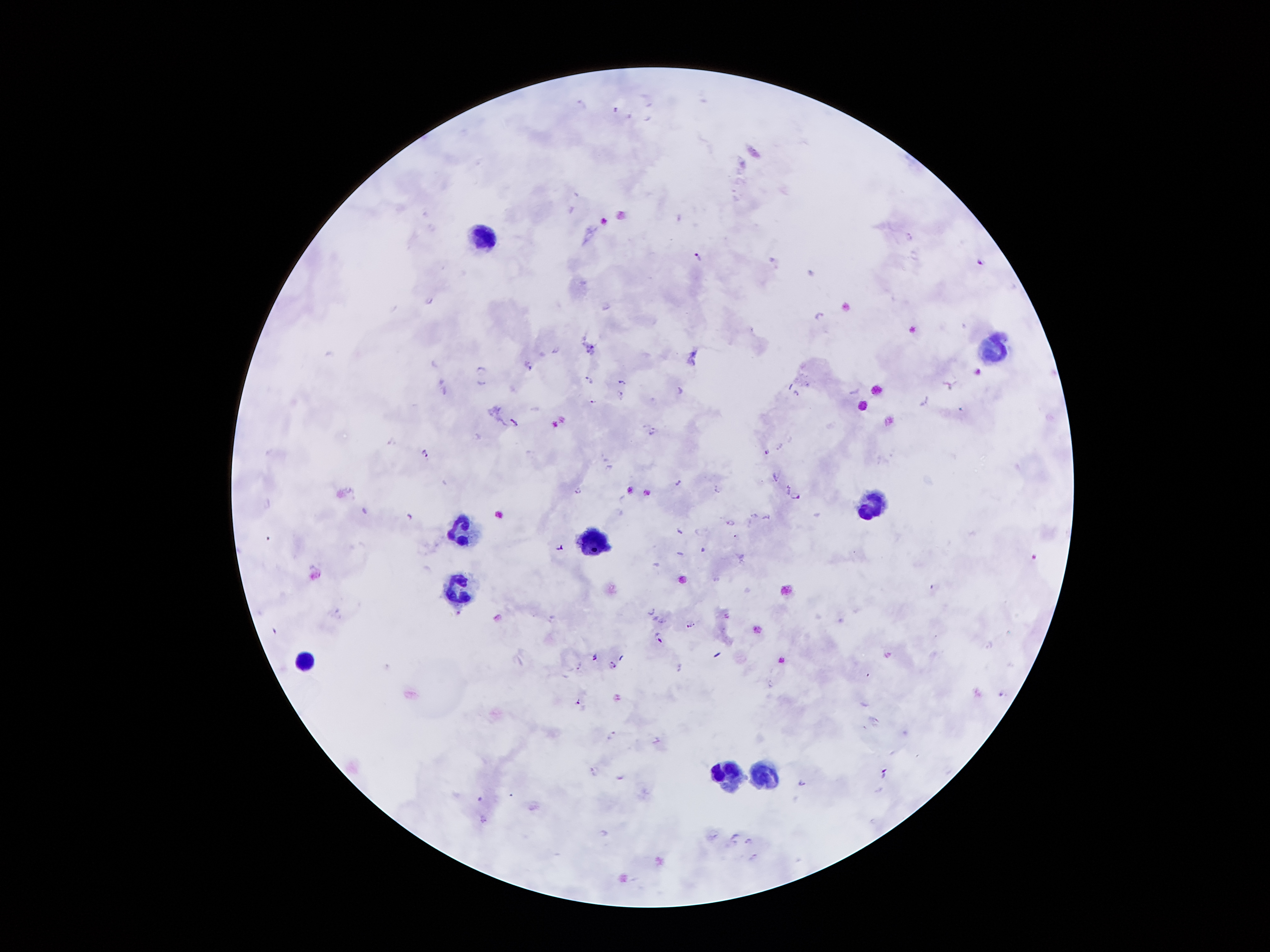
Approximate centers as {x, y} in pixels.
Summary:
  - Leukocyte locations: {483, 240}, {992, 347}, {869, 505}, {460, 529}, {592, 540}, {454, 587}, {303, 662}, {766, 773}, {729, 774}
  - Plasmodium parasite locations: {910, 236}, {697, 255}, {979, 262}, {429, 298}, {818, 314}, {529, 365}, {481, 368}, {440, 379}, {589, 379}, {620, 381}, {481, 384}, {948, 384}, {680, 386}, {444, 391}, {620, 392}, {795, 392}, {923, 400}, {593, 402}, {515, 421}, {651, 430}, {424, 451}, {766, 452}, {608, 467}, {776, 477}, {676, 482}, {717, 488}, {578, 489}, {788, 489}, {796, 496}, {407, 514}, {754, 514}, {766, 516}, {729, 522}, {679, 531}, {561, 546}, {651, 610}, {458, 613}, {726, 615}, {497, 616}, {662, 619}, {690, 625}, {658, 636}, {594, 655}, {613, 664}, {579, 665}, {679, 667}, {1000, 694}, {577, 701}, {611, 732}, {656, 740}, {592, 769}, {882, 773}, {618, 777}, {801, 781}, {483, 818}, {714, 835}, {734, 836}, {748, 840}, {753, 857}
  - Image size: 1270×952 pixels
  - Preparation: thick blood film
  - Magnification: 100x
  - Stain: Giemsa
  - Capture: smartphone through the microscope eyepiece
  - Patient malaria status: positive for Plasmodium falciparum
  - Field of view: one from this slide